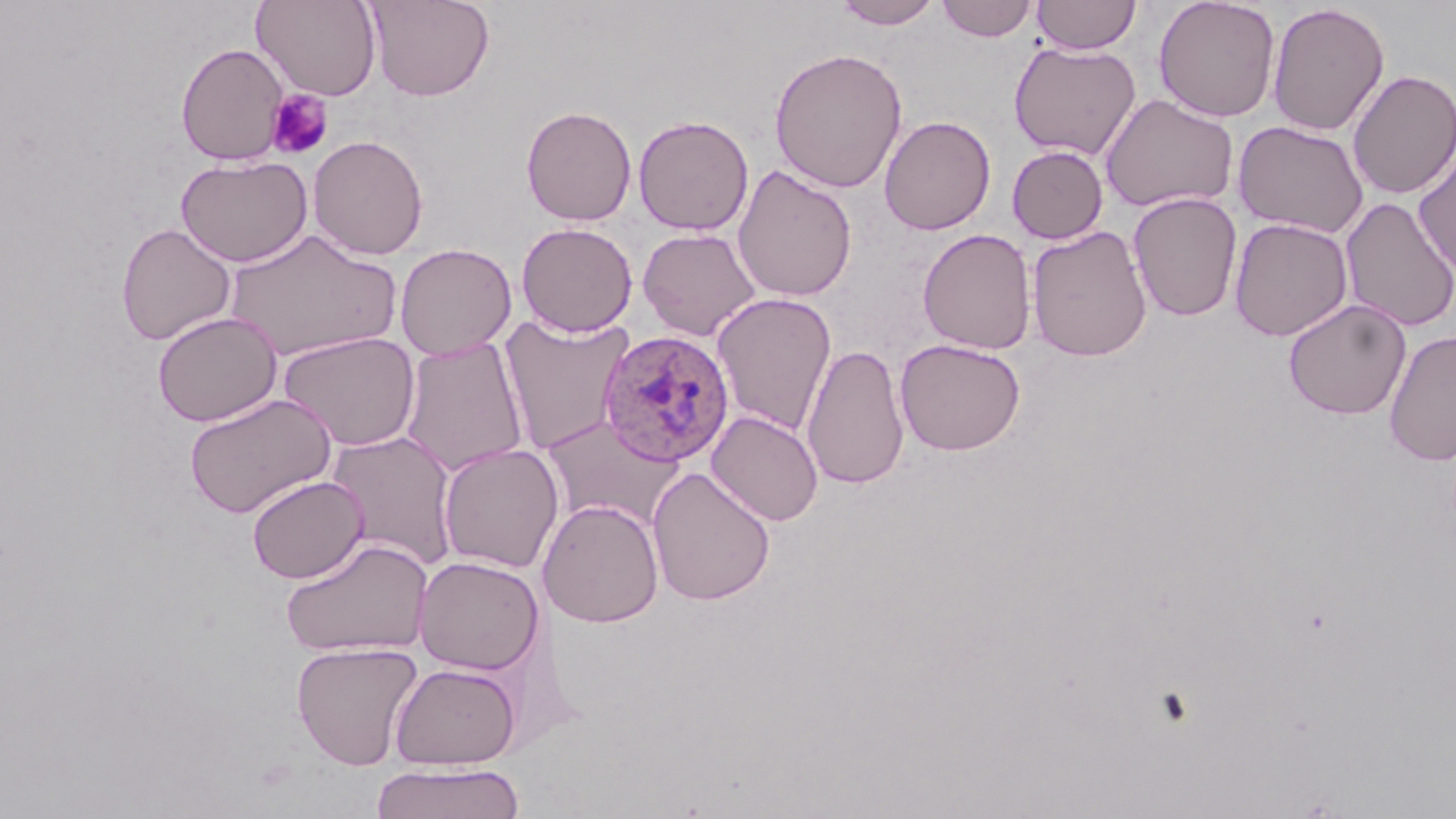

Summary:
  - Coordinate format: approximate bounding boxes as (x1,y1)-(x2,y2) corner pairs in pixels
  - Uninfected red blood cell locations: (252,0)-(382,101), (366,0)-(494,101), (833,0)-(943,29), (936,0)-(1037,41), (1031,0)-(1141,55), (1153,0)-(1281,122), (1266,3)-(1390,137), (175,41)-(289,166), (1008,41)-(1141,160), (769,47)-(908,193), (1347,68)-(1456,200), (1099,93)-(1239,214), (520,104)-(637,226), (633,114)-(754,236), (879,115)-(996,235), (1233,121)-(1369,239), (308,135)-(429,260), (1007,145)-(1109,244), (1413,149)-(1456,277), (175,154)-(312,267), (732,163)-(857,302), (1128,192)-(1243,322), (1339,196)-(1456,332), (1229,217)-(1354,342), (115,222)-(237,346), (516,222)-(638,337), (1026,226)-(1153,362), (637,228)-(761,341), (917,228)-(1037,354), (222,229)-(403,362), (394,243)-(517,360), (711,292)-(837,436), (1283,298)-(1411,420), (152,311)-(282,427), (499,313)-(635,454), (1384,329)-(1456,467), (278,331)-(421,451), (399,338)-(529,477), (894,338)-(1026,455), (801,343)-(910,490), (183,392)-(337,519), (706,411)-(823,526), (540,416)-(683,531), (325,429)-(461,572), (437,443)-(564,573), (647,466)-(776,606), (246,474)-(369,584), (538,498)-(664,628), (279,536)-(433,659), (413,556)-(544,675), (291,641)-(423,770), (389,662)-(521,769), (370,762)-(524,819)
  - Platelet locations: (266,90)-(333,160)
  - Plasmodium ovale-infected red blood cell locations: (597,329)-(735,467)
  - Slide-level diagnosis: Plasmodium ovale
  - Magnification: 1000x
  - Stain: May-Grünwald-Giemsa
  - Field of view: single
  - Modality: light microscopy
  - Preparation: thin blood smear
  - Image size: 1456×819 pixels